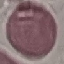

Malaria status: uninfected. Thin blood film. Automatically extracted cell patch, resized to 64 × 64 pixels. Photographed with a smartphone camera at the microscope eyepiece. Giemsa-stained preparation.